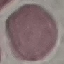

Summary:
  - Result: negative for malaria parasites
  - Capture: smartphone through the microscope eyepiece
  - Preparation: thin blood smear
  - Stain: Giemsa
  - Image type: cell patch, automatically extracted from a larger field of view and resized to 64 × 64 pixels